Classify this cell by malaria status.
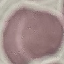
Uninfected.

Summary:
  - Preparation: thin smear
  - Image type: cell patch, automatically extracted from a larger field of view and resized to 64 × 64 pixels
  - Capture: smartphone through the microscope eyepiece
  - Stain: Giemsa